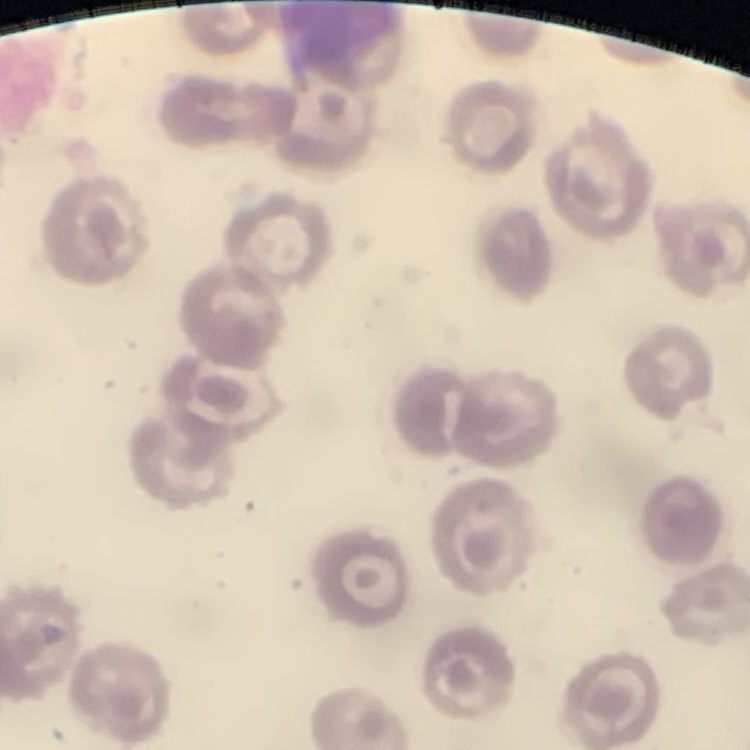

Summary:
  - Erythrocyte morphology: no rouleaux formation
  - Preparation: thin peripheral smear
  - Image type: one tile cut from a larger photomicrograph
  - Stain: Field's or Giemsa